Report the malaria status of this cell.
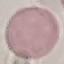
It is uninfected.

Summary:
  - Capture: smartphone camera at the microscope eyepiece
  - Stain: Giemsa
  - Image type: cell patch, automatically extracted from a larger field of view and resized to 64 × 64 pixels
  - Preparation: thin blood smear